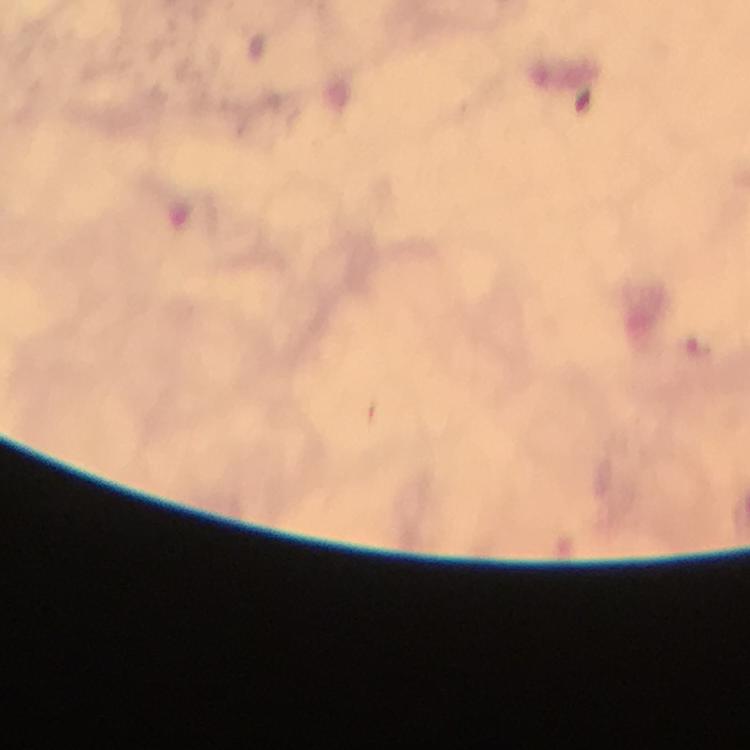
preparation = thick blood film
magnification = 100x
malaria parasite locations = approximate object centers, in pixels from the top-left corner: (x=698, y=348)
cropped from = one field of view
capture = smartphone mounted on the microscope
context = from a diagnostic examination for malaria
immersion oil = applied
stain = Giemsa
image size = 750×750 pixels